Classify this cell by malaria status.
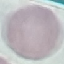

Uninfected.

preparation = thin blood film
stain = Giemsa
capture = smartphone through the microscope eyepiece
image type = cell patch, automatically extracted from a larger field of view and resized to 64 × 64 pixels